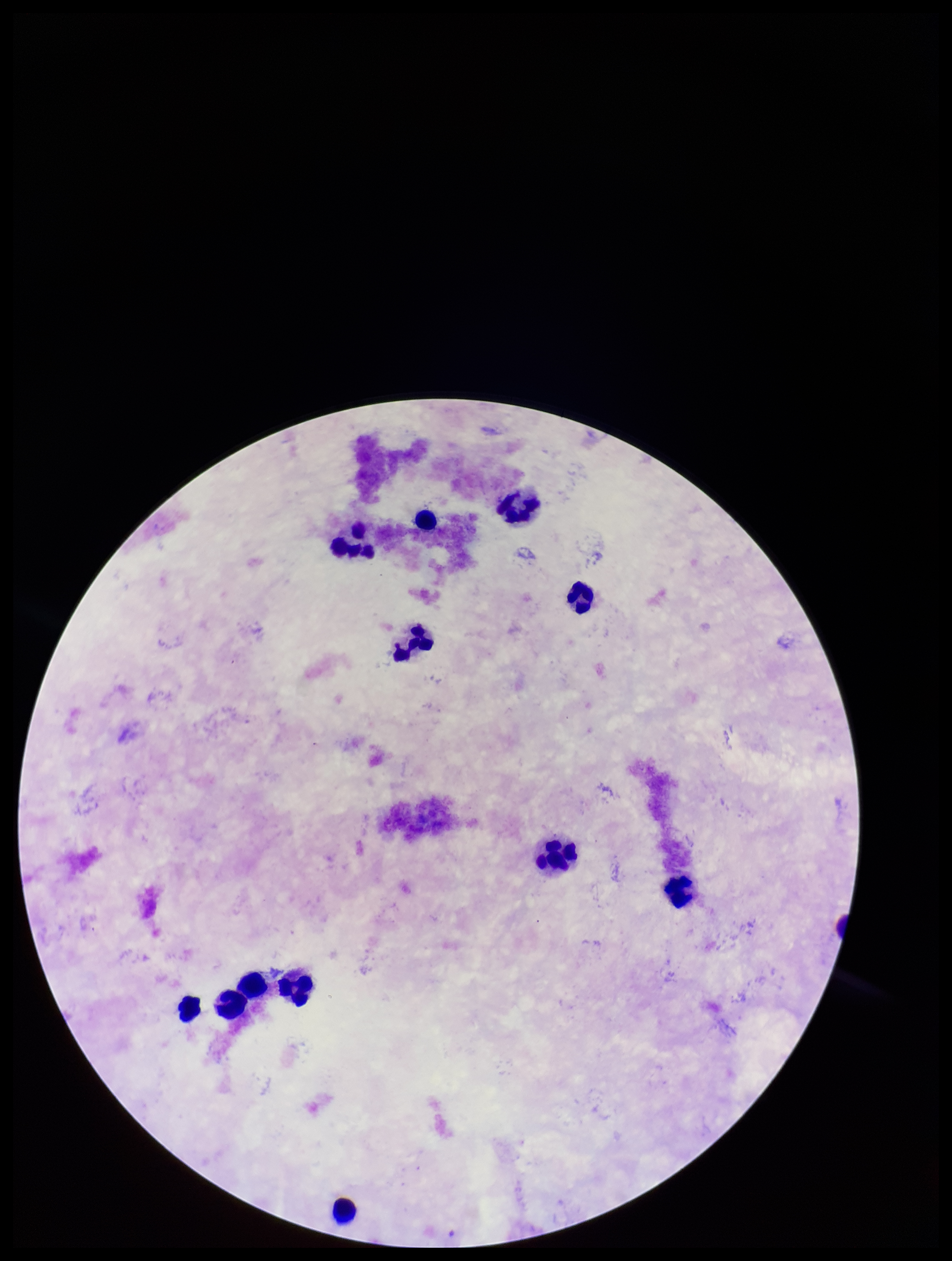

{
  "patient_malaria_status": "negative",
  "plasmodium_parasites": "none detected",
  "image_size": "952×1261 pixels",
  "parasite_count": 0,
  "capture": "smartphone photograph through the microscope eyepiece",
  "field_of_view": "single",
  "preparation": "thick",
  "stain": "Giemsa",
  "leukocyte_count": 12
}